Name the parasite shown.
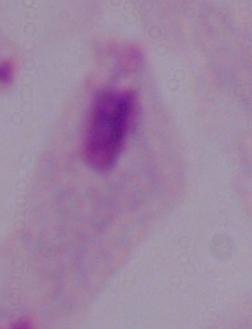
This is a trichomonad.

Summary:
  - Magnification: 1000x
  - Modality: photomicrograph